Locate every Plasmodium falciparum parasite and identify its life-cycle stage.
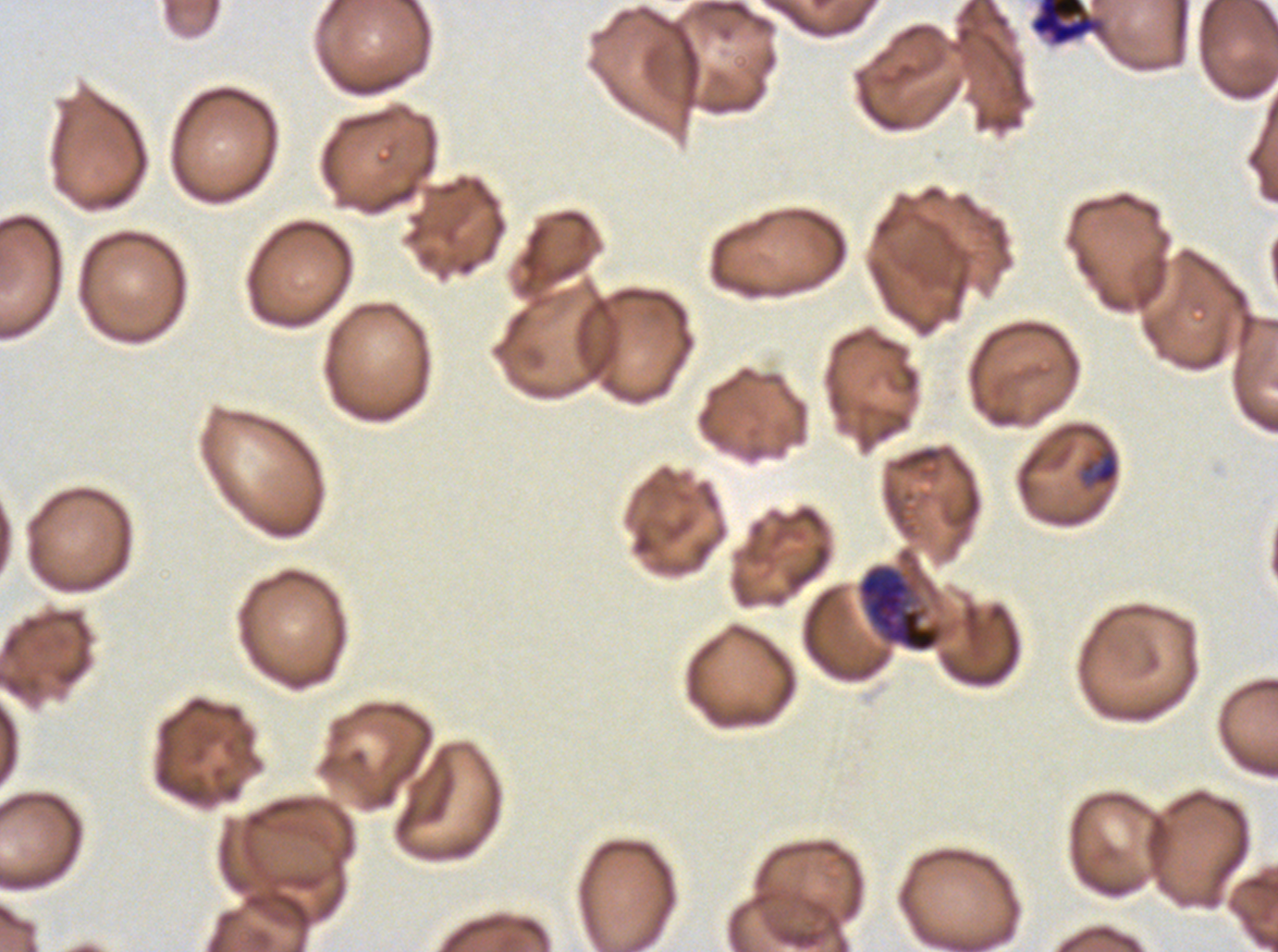

Approximate bounding boxes as [x1, y1, x2, y2] in pixels.
Late-ring/early-trophozoite forms: [1081, 446, 1119, 486].
Early schizonts: [856, 563, 946, 653].
Segmenters: [1030, 0, 1105, 46].
No rings, mid trophozoites, late trophozoites, late schizonts, or gametocytes observed.

One sub-image of a larger composite. Giemsa-stained preparation. Life-cycle stages observed: late-ring/early-trophozoite, early schizont, segmenter. Plasmodium falciparum cultured ex vivo for 24 to 48 hours, from a patient in The Gambia. Thin blood smear. Image is 1278×952 pixels.